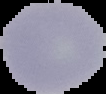

Summary:
  - Image size: 106×94 pixels
  - Malaria status: uninfected
  - Preparation: thin blood smear
  - Image type: segmented cell region on a black background